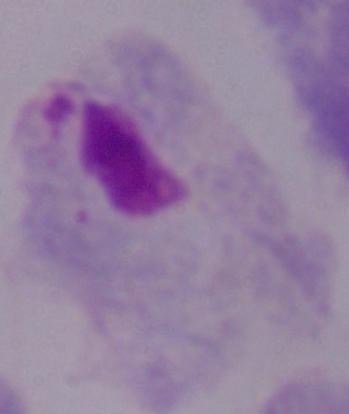
1000x magnification. A trichomonad is shown. Micrograph.